Assess the morphology of the red blood cells.
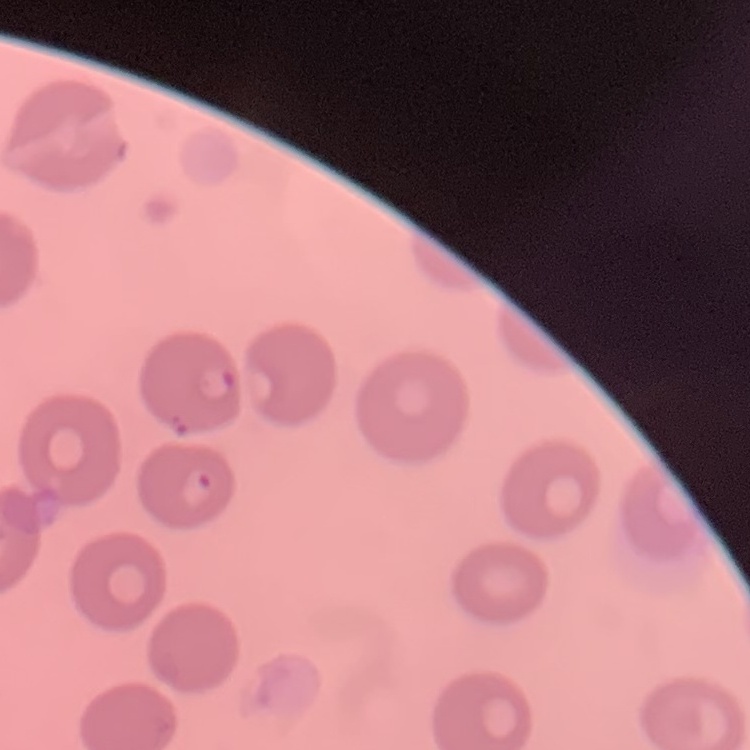

They show no rouleaux formation.

image type = square crop of a larger photomicrograph
preparation = thin peripheral smear
stain = Field's or Giemsa